Evaluate for malaria.
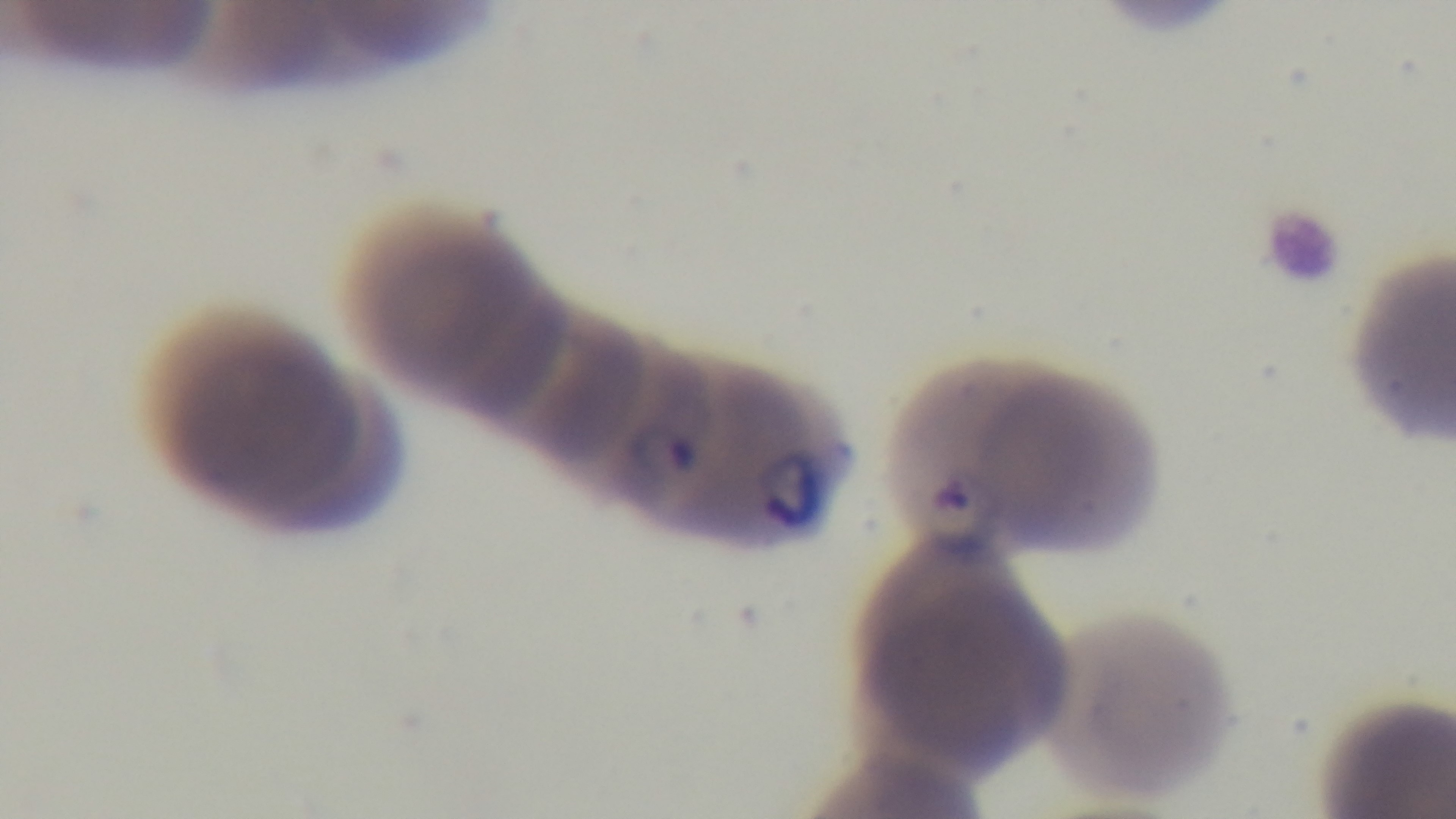

Infected.

Photomicrograph. 100x oil-immersion objective. One field from the slide. Captured with a mounted 4K digital camera. Preparation: thin blood film. Giemsa-stained.